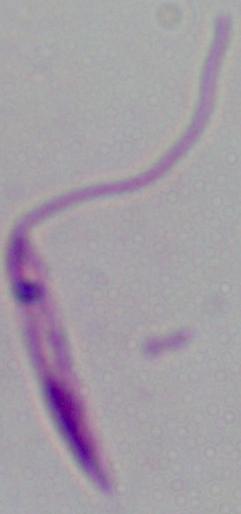

Summary:
  - Identification: Leishmania
  - Magnification: 1000x
  - Modality: photomicrograph